Identify the blood parasite species.
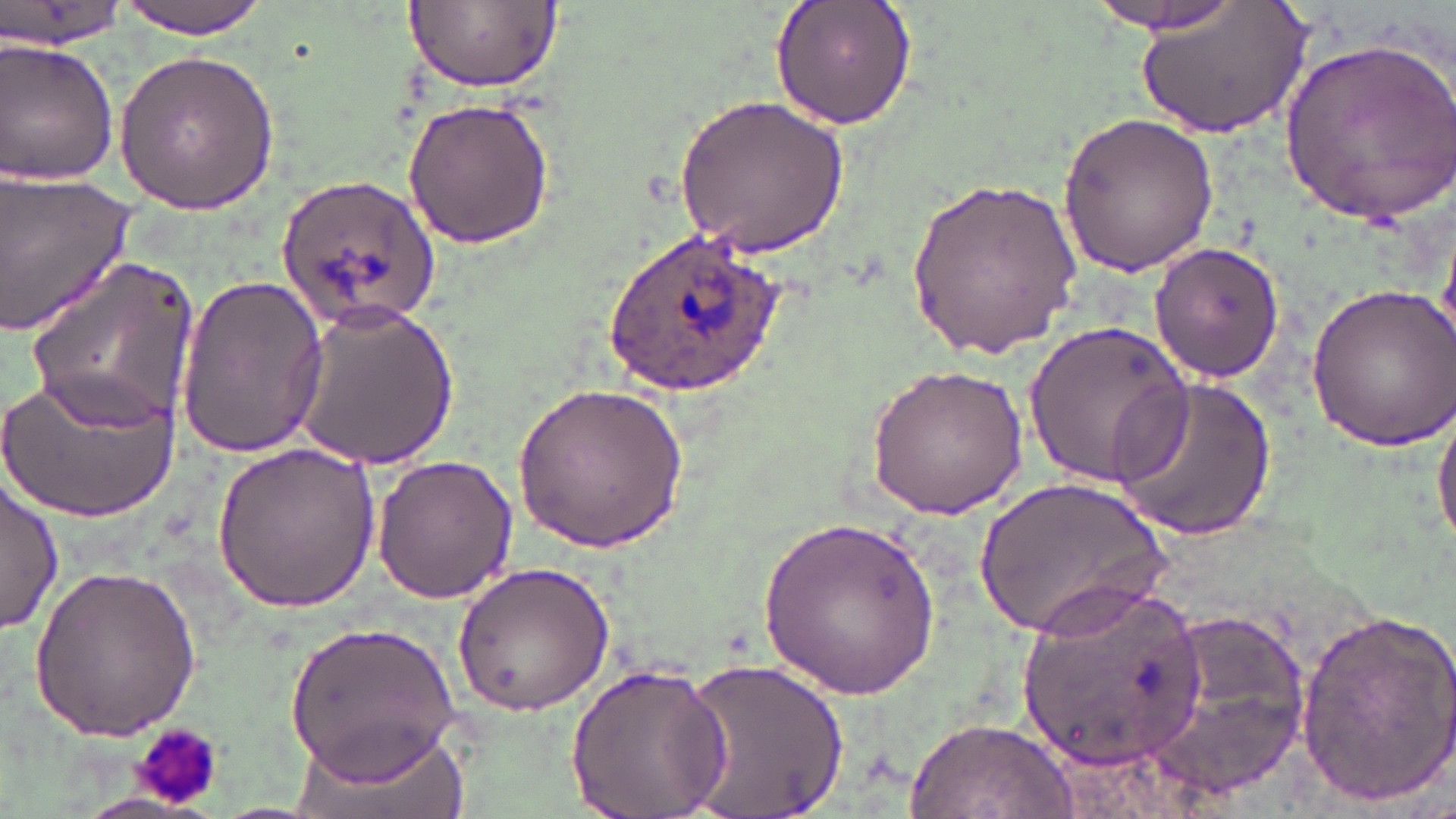

Plasmodium ovale.

Approximate bounding boxes as (x1,y1)-(x2,y2) corner pairs in pixels. Uninfected red blood cell locations: (0,0)-(128,50), (114,0)-(276,37), (404,0)-(560,93), (770,0)-(918,131), (1083,0)-(1254,38), (1138,0)-(1310,140), (0,35)-(122,185), (1280,36)-(1454,228), (113,49)-(278,213), (674,92)-(850,259), (403,97)-(555,249), (1057,110)-(1219,277), (0,168)-(140,339), (906,173)-(1081,358), (1148,241)-(1285,382), (27,258)-(200,436), (172,270)-(329,460), (1303,280)-(1454,454), (290,302)-(459,469), (1026,319)-(1192,490), (864,362)-(1028,518), (3,367)-(178,523), (1109,375)-(1277,542), (514,381)-(687,555), (1432,398)-(1456,553), (211,440)-(383,609), (370,454)-(517,604), (974,473)-(1171,642), (1,476)-(63,633), (759,513)-(939,700), (30,559)-(203,742), (449,559)-(618,716), (1014,578)-(1210,776), (1144,607)-(1317,797), (1294,608)-(1456,810), (285,617)-(461,780), (679,653)-(852,819), (564,659)-(732,819), (903,716)-(1077,819), (285,719)-(466,819). Plasmodium ovale-infected red blood cell locations: (276,172)-(441,333), (605,227)-(787,394). Platelet locations: (135,725)-(226,809). Image is 1456×819 pixels. Optical microscopy. Thin blood smear. Single field of view. May-Grünwald-Giemsa-stained preparation. Captured at 1000x magnification.